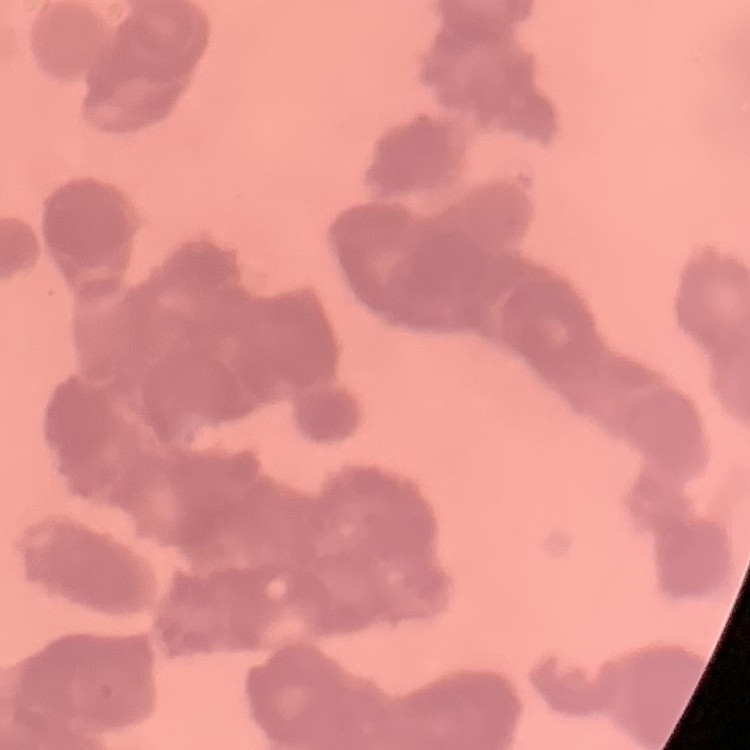
red_blood_cell_morphology: rouleaux formation
stain: Field's or Giemsa
image_type: one tile cut from a larger photomicrograph
preparation: thin blood smear